Classify this cell by malaria status.
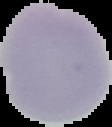

Uninfected.

Summary:
  - Preparation: thin blood smear
  - Image type: cell region segmented out of the field of view; surrounding area masked to black
  - Image size: 112×127 pixels